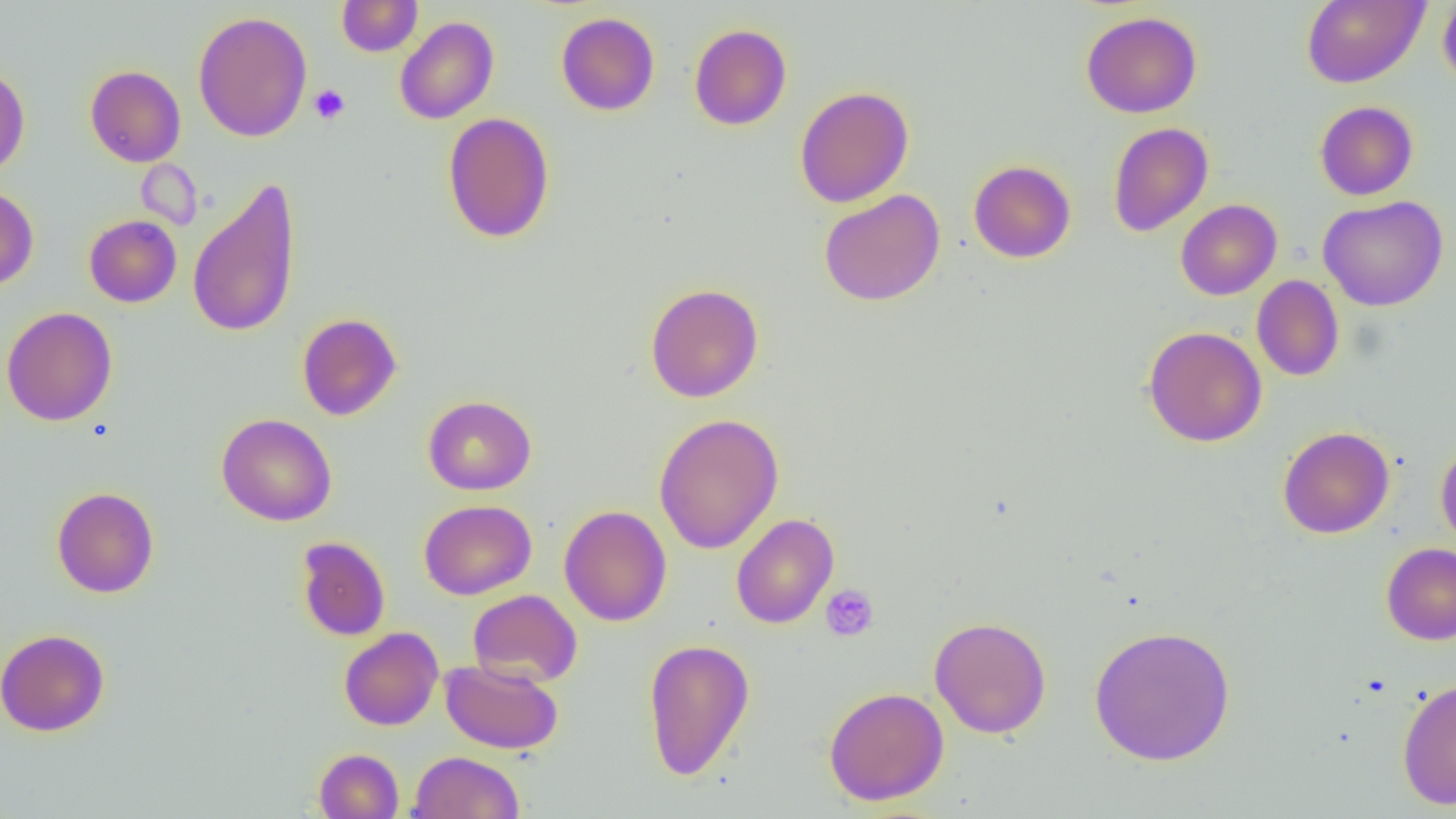

slide-level diagnosis = negative for blood parasites
image size = 1456×819 pixels
modality = optical microscopy
preparation = thin blood film
uninfected red blood cell locations = approximate bounding boxes as named x1/y1/x2/y2 corners in pixels: (x1=337, y1=0, x2=422, y2=56), (x1=1301, y1=0, x2=1428, y2=88), (x1=1438, y1=0, x2=1456, y2=90), (x1=193, y1=11, x2=312, y2=142), (x1=1081, y1=11, x2=1202, y2=118), (x1=556, y1=12, x2=660, y2=116), (x1=394, y1=16, x2=499, y2=124), (x1=689, y1=24, x2=792, y2=130), (x1=0, y1=63, x2=30, y2=179), (x1=85, y1=65, x2=186, y2=167), (x1=794, y1=86, x2=914, y2=208), (x1=1314, y1=100, x2=1418, y2=201), (x1=442, y1=112, x2=555, y2=243), (x1=1107, y1=122, x2=1214, y2=237), (x1=968, y1=160, x2=1076, y2=263), (x1=187, y1=177, x2=302, y2=339), (x1=0, y1=185, x2=38, y2=292), (x1=819, y1=189, x2=945, y2=306), (x1=1318, y1=195, x2=1449, y2=312), (x1=1175, y1=199, x2=1282, y2=300), (x1=84, y1=215, x2=182, y2=307), (x1=1251, y1=275, x2=1344, y2=381), (x1=645, y1=283, x2=764, y2=403), (x1=1, y1=306, x2=118, y2=426), (x1=297, y1=313, x2=402, y2=420), (x1=1143, y1=326, x2=1267, y2=447), (x1=423, y1=395, x2=536, y2=495), (x1=653, y1=412, x2=784, y2=554), (x1=216, y1=413, x2=337, y2=526), (x1=1278, y1=426, x2=1394, y2=539), (x1=1435, y1=441, x2=1456, y2=550), (x1=51, y1=486, x2=159, y2=598), (x1=418, y1=499, x2=537, y2=600), (x1=559, y1=505, x2=672, y2=626), (x1=731, y1=513, x2=839, y2=629), (x1=296, y1=536, x2=391, y2=641), (x1=1381, y1=543, x2=1456, y2=645), (x1=468, y1=589, x2=582, y2=688), (x1=929, y1=616, x2=1052, y2=739), (x1=1089, y1=624, x2=1236, y2=766), (x1=339, y1=627, x2=443, y2=730), (x1=0, y1=628, x2=110, y2=737), (x1=642, y1=638, x2=755, y2=780), (x1=440, y1=658, x2=564, y2=754), (x1=1397, y1=677, x2=1456, y2=810), (x1=823, y1=686, x2=950, y2=806), (x1=314, y1=748, x2=404, y2=819), (x1=408, y1=751, x2=524, y2=819)
field of view = single
magnification = 1000x
platelet locations = approximate bounding boxes as named x1/y1/x2/y2 corners in pixels: (x1=308, y1=84, x2=350, y2=125), (x1=820, y1=583, x2=879, y2=642)